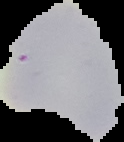

Malaria status: uninfected. Image is 124×142 pixels. From a thin blood film. The area outside the segmented cell region is set to black.